Give the extent of all Plasmodium parasites.
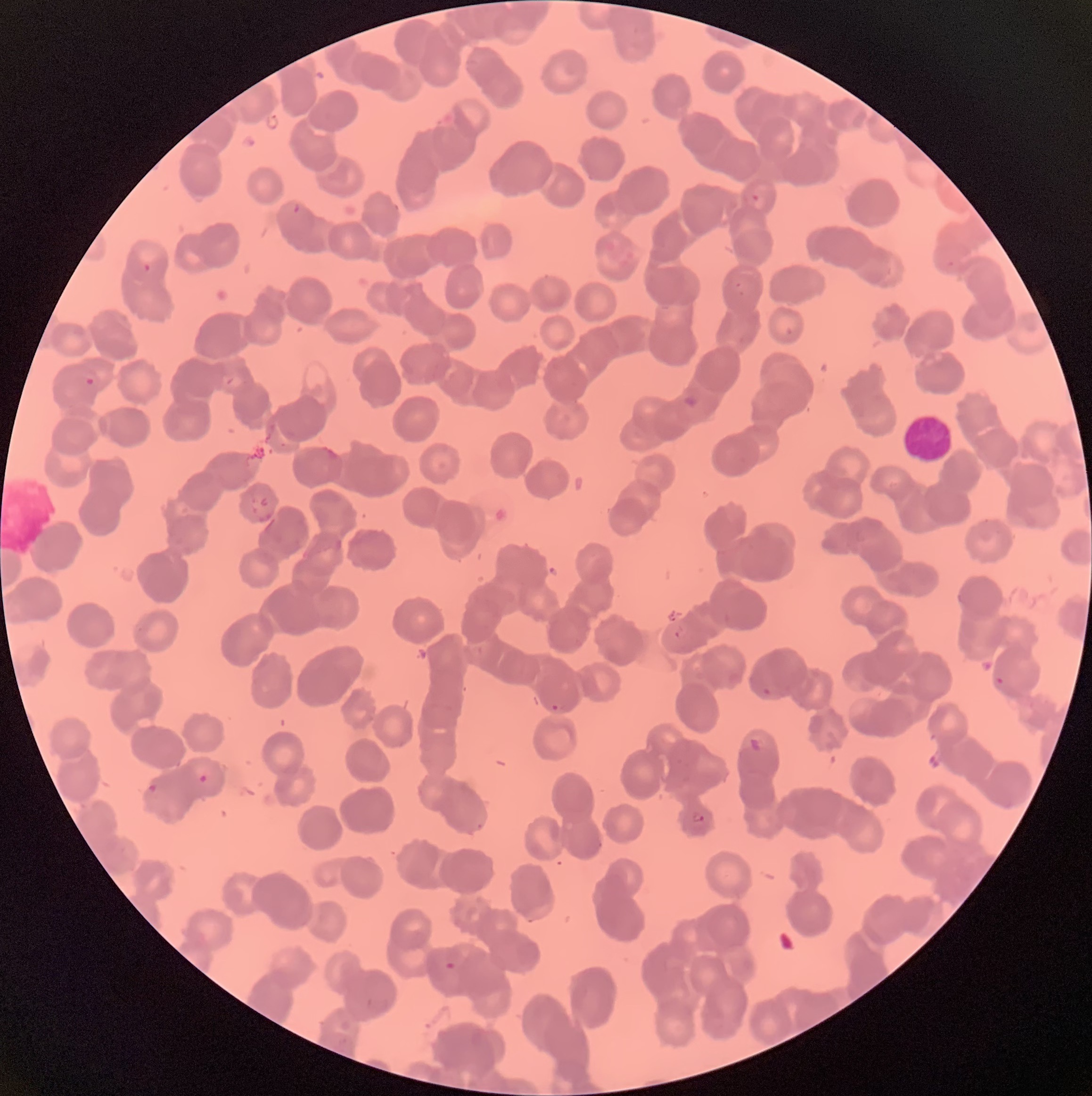

Approximate bounding boxes as (x1,y1)-(x2,y2) corner pairs in pixels.
Plasmodium parasites: (435,119)-(455,130), (586,171)-(596,181), (751,194)-(761,201), (291,203)-(302,214), (392,204)-(399,213), (141,263)-(153,273), (735,282)-(746,298), (784,325)-(796,337), (733,335)-(746,346), (85,377)-(96,386), (683,391)-(702,409), (672,625)-(686,638), (469,642)-(488,656), (994,676)-(1014,689), (760,686)-(775,698), (548,700)-(565,714), (191,764)-(212,784), (148,783)-(167,797), (691,811)-(707,825), (474,820)-(486,831), (597,840)-(603,850), (526,904)-(552,923), (442,961)-(458,972).

Summary:
  - White blood cell locations: (902,415)-(953,463)
  - Preparation: thin blood smear
  - Red blood cell morphology: rouleaux formation
  - Modality: light microscopy
  - Image size: 1092×1096 pixels